Name the blood parasite species.
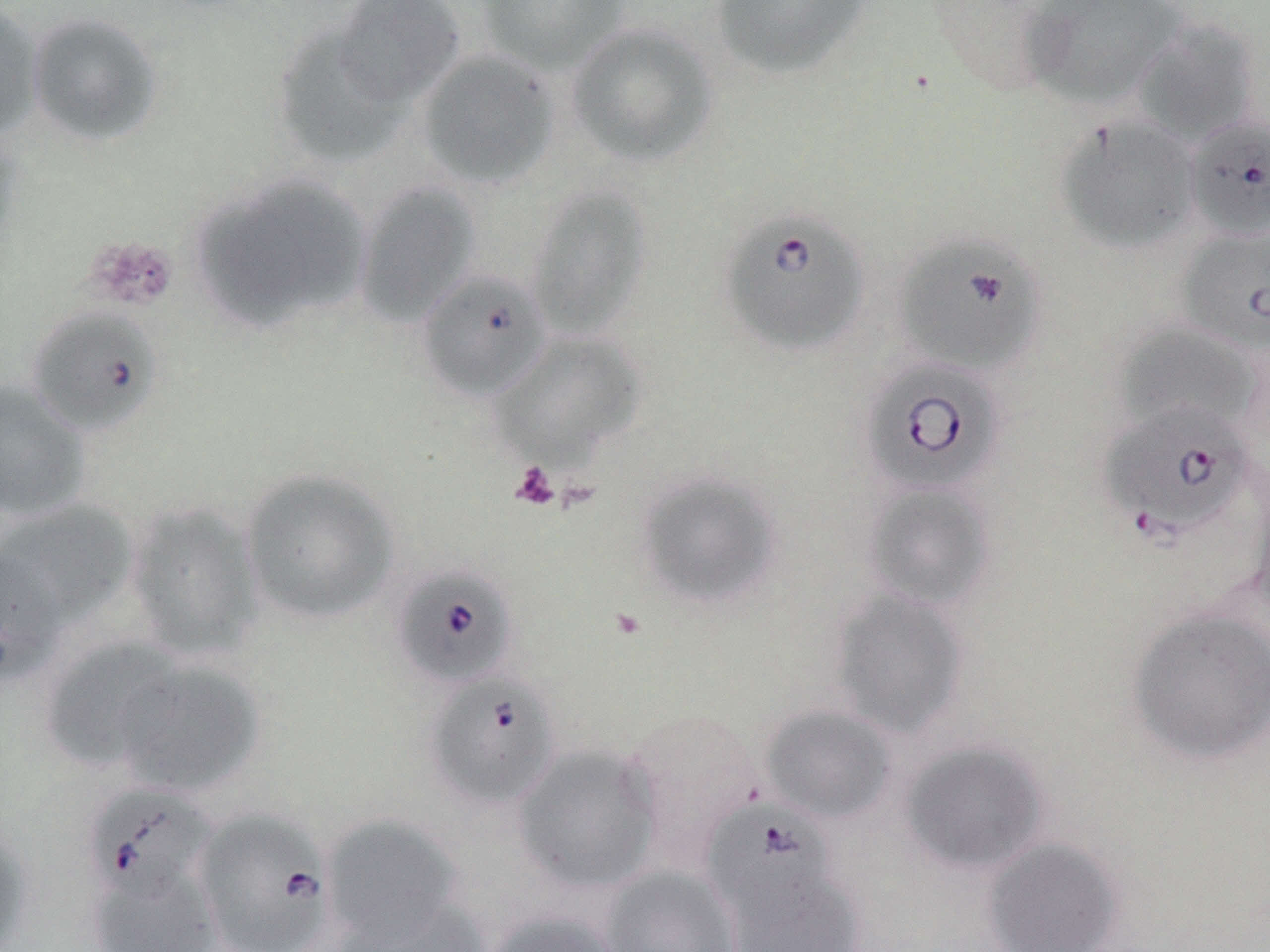
Babesia divergens.

Summary:
  - Coordinate format: approximate bounding boxes as (x1, y1, x2, y2) in pixels
  - Platelet locations: (84, 235, 179, 312), (509, 462, 560, 510)
  - Babesia divergens-infected red blood cell locations: (1185, 114, 1270, 241), (719, 206, 871, 357), (1177, 226, 1270, 355), (893, 234, 1046, 377), (415, 269, 551, 401), (26, 306, 163, 436), (858, 357, 1007, 498), (1098, 401, 1258, 543), (391, 563, 519, 690), (424, 672, 562, 810), (84, 784, 216, 903), (703, 800, 838, 920), (192, 807, 336, 952)
  - Uninfected red blood cell locations: (331, 0, 466, 106), (476, 0, 631, 74), (709, 0, 872, 80), (1018, 0, 1188, 110), (0, 3, 44, 141), (25, 12, 164, 146), (1132, 18, 1262, 145), (271, 21, 409, 170), (567, 22, 719, 167), (416, 50, 559, 190), (1055, 115, 1201, 253), (0, 126, 25, 265), (193, 175, 371, 332), (354, 181, 482, 327), (526, 184, 652, 340), (1114, 322, 1261, 438), (492, 331, 646, 469), (0, 380, 92, 522), (240, 468, 400, 625), (635, 469, 784, 610), (1245, 472, 1270, 623), (862, 482, 996, 612), (1, 500, 139, 628), (125, 501, 263, 660), (0, 545, 64, 689), (828, 589, 969, 737), (1127, 604, 1270, 765), (39, 636, 185, 774), (112, 660, 264, 797), (759, 704, 898, 824), (619, 708, 765, 860), (898, 740, 1049, 875), (512, 743, 662, 894), (321, 814, 465, 948), (0, 821, 36, 952), (981, 836, 1125, 952), (84, 864, 222, 951), (600, 865, 742, 952), (724, 867, 867, 952), (338, 897, 491, 952), (482, 910, 625, 952)
  - Stain: May-Grünwald-Giemsa
  - Magnification: 1000x
  - Modality: optical microscopy
  - Image size: 1270×952 pixels
  - Preparation: thin blood film
  - Field of view: one of a larger specimen